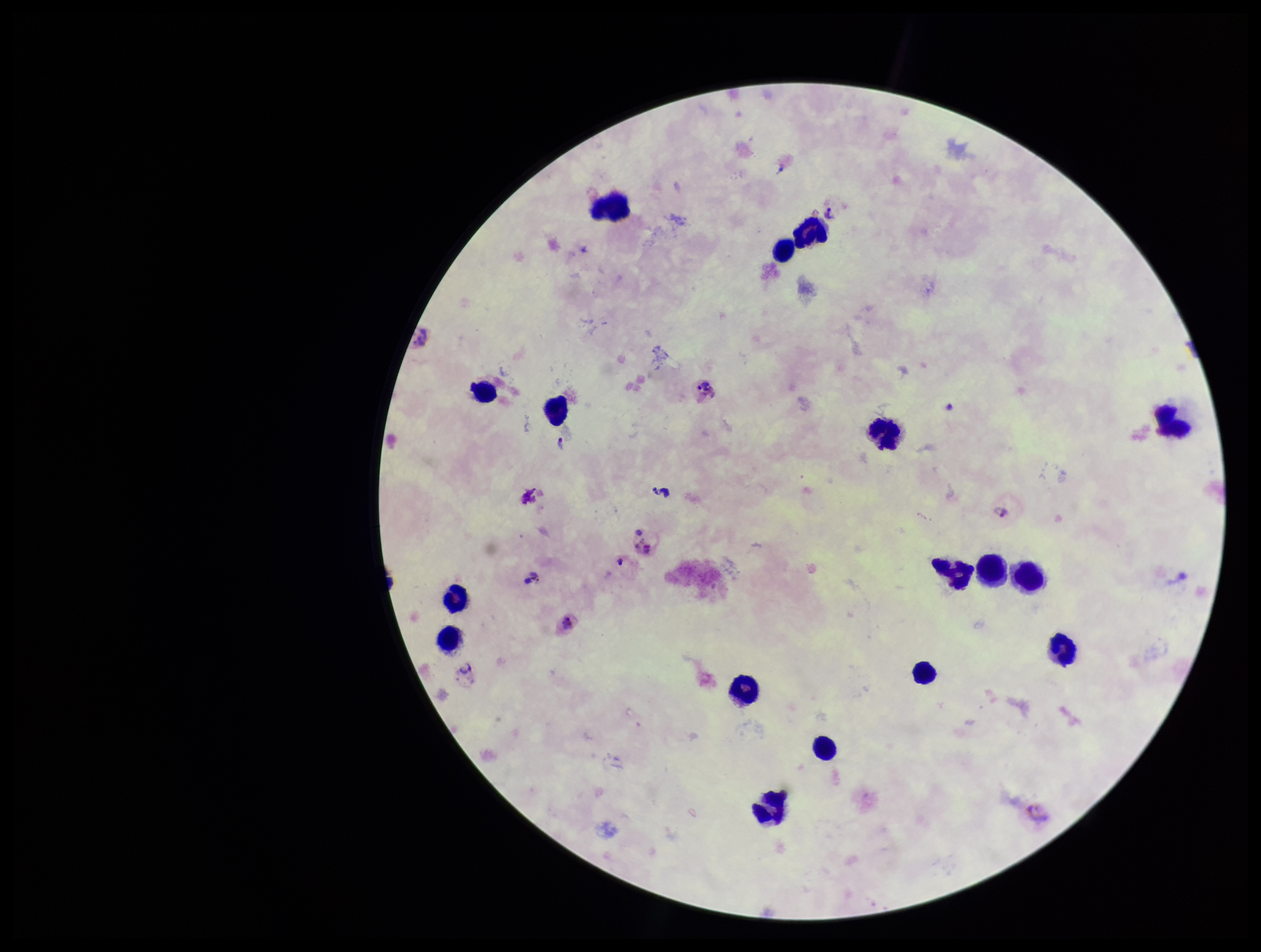

Summary:
  - Parasite count: 5
  - Image size: 1261×952 pixels
  - Patient malaria status: infected
  - Preparation: thick smear
  - Field of view: one from this slide
  - Plasmodium parasites: seen
  - Stain: Giemsa
  - Capture: smartphone photograph through the microscope eyepiece
  - Species reported for this patient: Plasmodium vivax
  - Leukocyte count: 17